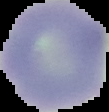

Summary:
  - Preparation: thin blood film
  - Image size: 109×112 pixels
  - Malaria status: uninfected
  - Image type: segmented cell region on a black background